Assess this cell for malaria.
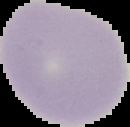

Uninfected.

{
  "image_type": "cell region segmented out of the field of view; surrounding area masked to black",
  "image_size": "130×127 pixels",
  "preparation": "thin blood film"
}